Assess this cell for malaria.
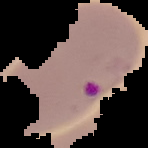
Parasitized.

image size = 148×148 pixels
preparation = thin blood smear
image type = cell region segmented out of the field of view; surrounding area masked to black